Assess this cell for malaria.
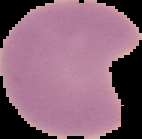
It is parasitized.

image size = 142×139 pixels
image type = segmented cell region with the area outside set to black
preparation = thin blood smear